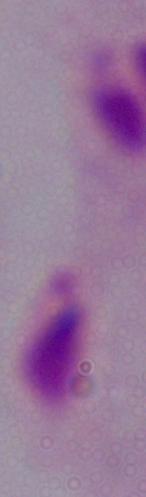
Photomicrograph. A trichomonad is seen. Captured at 1000x magnification.